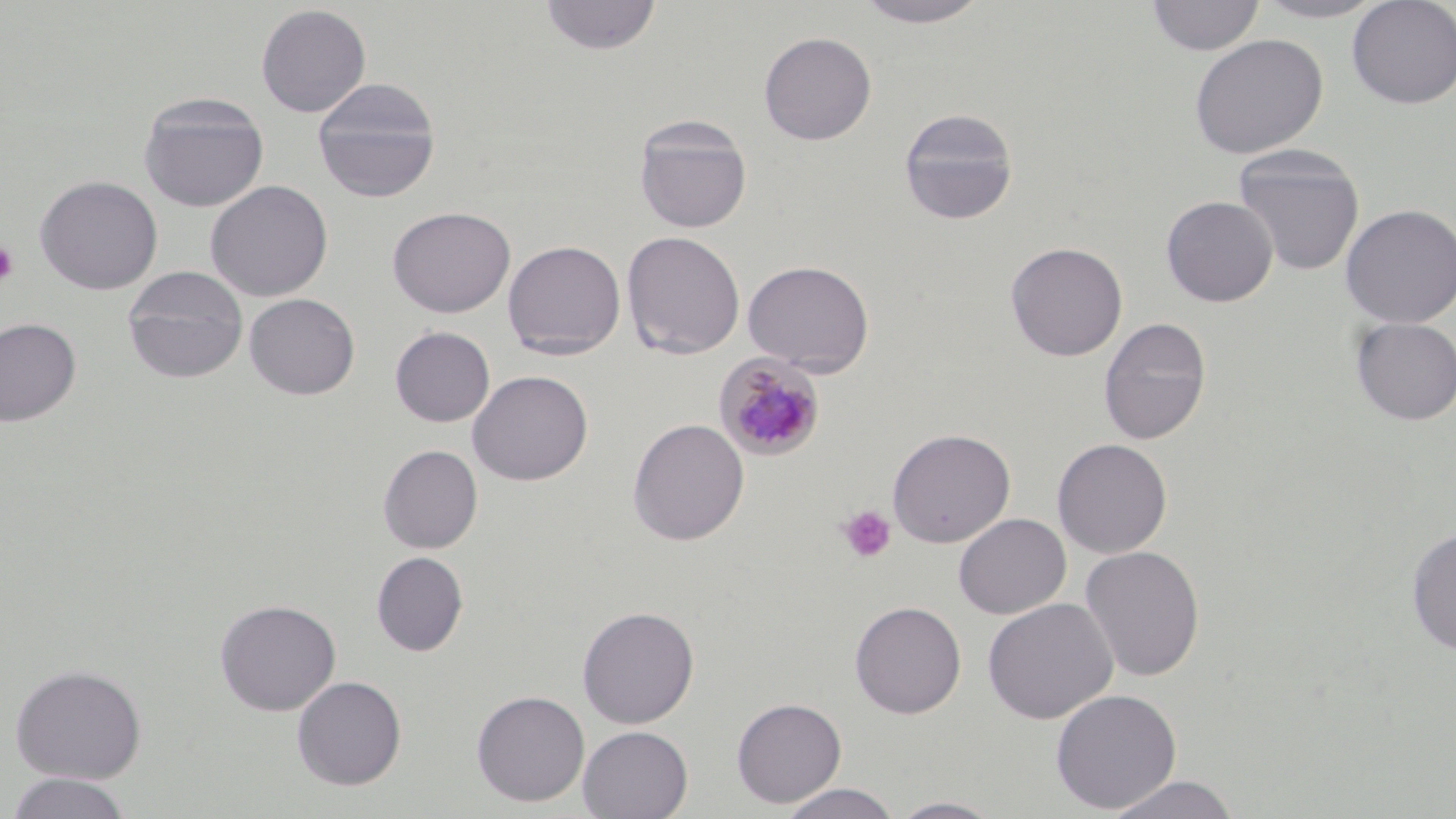

Approximate bounding boxes as [x1, y1, x2, y2] in pixels. Platelet locations: [0, 241, 18, 287], [837, 505, 895, 562]. Plasmodium malariae-infected red blood cell locations: [714, 353, 826, 461]. Uninfected red blood cell locations: [539, 0, 662, 56], [852, 0, 995, 28], [1146, 0, 1264, 57], [1250, 0, 1390, 23], [1346, 0, 1456, 109], [255, 4, 371, 117], [758, 31, 877, 145], [1189, 33, 1328, 159], [312, 78, 441, 202], [138, 94, 269, 212], [897, 108, 1020, 226], [633, 115, 753, 234], [1232, 146, 1365, 276], [34, 174, 163, 295], [205, 179, 333, 301], [1160, 195, 1278, 307], [1340, 203, 1456, 328], [387, 206, 516, 318], [621, 231, 745, 359], [503, 240, 626, 360], [1005, 241, 1128, 361], [742, 259, 874, 376], [122, 266, 249, 383], [243, 293, 360, 400], [1350, 316, 1456, 426], [0, 317, 82, 426], [1098, 317, 1211, 445], [390, 326, 495, 427], [467, 369, 593, 486], [627, 418, 749, 546], [887, 428, 1016, 548], [1052, 438, 1173, 558], [378, 444, 483, 553], [953, 513, 1071, 619], [1405, 527, 1456, 655], [1079, 545, 1205, 682], [371, 551, 469, 656], [982, 597, 1118, 724], [214, 598, 341, 716], [849, 600, 966, 718], [577, 606, 699, 728], [9, 663, 147, 783], [292, 675, 406, 790], [1050, 688, 1182, 814], [471, 689, 590, 807], [731, 696, 846, 808], [577, 725, 693, 818], [4, 772, 134, 818], [1102, 775, 1240, 818], [777, 783, 902, 819], [887, 796, 1005, 818]. Slide-level diagnosis: Plasmodium malariae. Thin blood film. May-Grünwald-Giemsa-stained preparation. Image is 1456×819 pixels. Light microscopy. Captured at 1000x magnification. One field of a larger specimen.